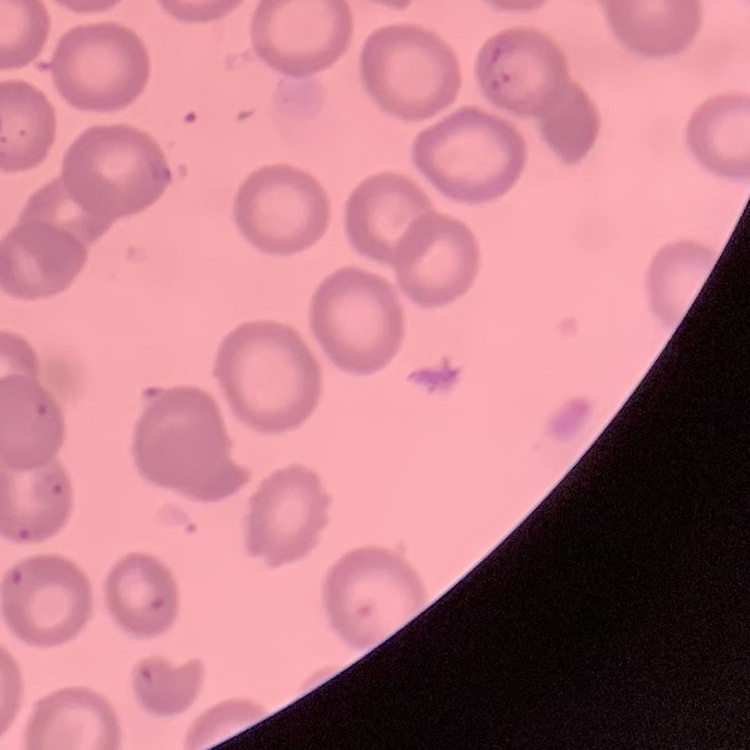

erythrocyte morphology = no rouleaux formation
image type = one tile cut from a larger photomicrograph
preparation = thin blood smear
stain = Field's or Giemsa